Report the malaria status of this cell.
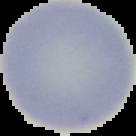

It is uninfected.

Summary:
  - Image type: segmented cell region with the area outside set to black
  - Preparation: thin blood smear
  - Image size: 136×136 pixels